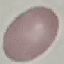
Malaria status: uninfected. Giemsa stain. Acquired by smartphone through the microscope eyepiece. Thin blood film. Automatically extracted cell patch, resized to 64 × 64 pixels.